Point out each malaria parasite and each leukocyte.
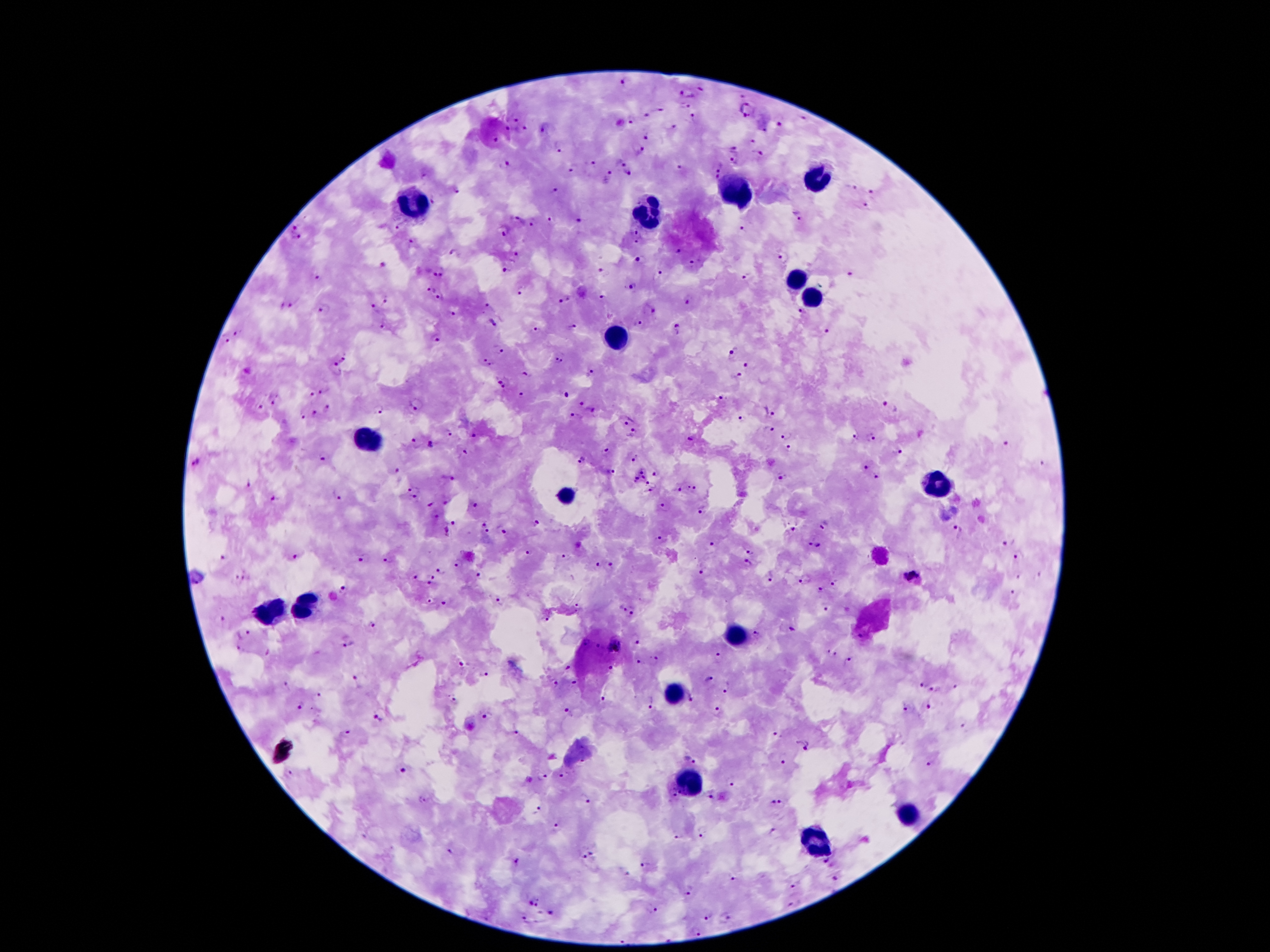
Approximate centers as [x, y] in pixels.
Malaria parasites: [627, 80], [702, 89], [688, 92], [739, 96], [685, 107], [748, 110], [664, 111], [647, 118], [805, 118], [515, 119], [632, 120], [694, 120], [781, 125], [672, 127], [506, 128], [544, 128], [522, 129], [647, 136], [496, 140], [751, 142], [558, 147], [734, 149], [640, 151], [758, 153], [621, 161], [734, 161], [593, 163], [503, 164], [718, 164], [574, 166], [677, 169], [629, 174], [424, 176], [607, 177], [714, 179], [852, 188], [457, 190], [557, 191], [873, 192], [435, 200], [866, 206], [798, 215], [518, 218], [552, 220], [580, 220], [532, 222], [399, 227], [504, 230], [742, 231], [297, 233], [639, 236], [411, 243], [676, 252], [455, 253], [516, 253], [783, 257], [640, 261], [383, 266], [695, 266], [506, 270], [603, 270], [439, 271], [662, 274], [849, 275], [750, 276], [321, 278], [634, 285], [431, 288], [520, 289], [441, 297], [602, 299], [688, 299], [386, 300], [564, 300], [295, 303], [488, 304], [280, 306], [374, 307], [326, 308], [651, 310], [803, 312], [454, 313], [493, 322], [385, 324], [639, 325], [570, 326], [677, 330], [535, 331], [239, 332], [824, 333], [226, 339], [437, 339], [499, 350], [732, 350], [343, 359], [560, 359], [748, 360], [489, 361], [335, 369], [592, 372], [525, 375], [736, 376], [503, 383], [326, 389], [524, 394], [311, 396], [564, 396], [723, 398], [276, 401], [419, 402], [582, 405], [260, 407], [329, 407], [890, 408], [592, 409], [377, 410], [772, 410], [316, 416], [576, 417], [301, 418], [626, 419], [744, 419], [769, 428], [450, 434], [633, 434], [785, 435], [474, 436], [854, 437], [692, 438], [870, 438], [418, 443], [432, 444], [1007, 444], [790, 450], [608, 452], [899, 452], [465, 453], [636, 456], [326, 457], [582, 461], [195, 462], [1041, 465], [866, 468], [643, 469], [398, 471], [611, 472], [657, 473], [782, 475], [877, 477], [448, 478], [643, 478], [636, 479], [652, 484], [695, 487], [680, 488], [415, 490], [337, 493], [649, 493], [273, 500], [448, 501], [431, 503], [477, 503], [664, 506], [702, 510], [481, 523], [534, 524], [824, 525], [450, 529], [792, 529], [505, 530], [958, 530], [490, 531], [661, 537], [1003, 544], [713, 545], [813, 545], [750, 551], [530, 552], [1019, 556], [566, 557], [295, 558], [362, 558], [222, 559], [390, 559], [458, 563], [598, 563], [748, 563], [612, 565], [440, 570], [702, 571], [910, 575], [481, 576], [772, 576], [416, 577], [432, 577], [1018, 577], [1040, 577], [240, 578], [805, 579], [836, 582], [431, 584], [345, 588], [822, 589], [1012, 593], [499, 599], [429, 602], [445, 604], [578, 606], [825, 608], [622, 609], [633, 611], [548, 616], [221, 618], [373, 622], [791, 628], [243, 632], [756, 633], [860, 635], [635, 638], [348, 642], [585, 642], [614, 645], [596, 647], [240, 649], [833, 653], [718, 658], [638, 661], [654, 661], [847, 661], [462, 664], [610, 668], [567, 669], [486, 675], [709, 680], [574, 682], [356, 683], [920, 683], [556, 685], [288, 686], [956, 686], [728, 687], [936, 688], [320, 695], [604, 695], [452, 699], [693, 699], [652, 700], [299, 705], [929, 707], [568, 709], [718, 709], [909, 710], [486, 716], [379, 717], [347, 732], [514, 734], [777, 734], [802, 745], [690, 760], [582, 762], [784, 762], [929, 765], [403, 770], [291, 774], [564, 775], [541, 777], [731, 786], [672, 793], [709, 796], [585, 798], [422, 799], [773, 801], [782, 804], [539, 808], [559, 827], [702, 835], [676, 838], [587, 856], [515, 859], [827, 860], [646, 864], [624, 872], [733, 878], [835, 878], [791, 885], [689, 892], [795, 902], [534, 903], [654, 909], [551, 915], [708, 916], [725, 918], [525, 920], [697, 932].
Leukocytes: [815, 177], [734, 193], [409, 205], [647, 213], [795, 280], [811, 293], [615, 339], [372, 443], [938, 484], [566, 495], [302, 604], [275, 609], [736, 632], [674, 691], [692, 784], [910, 814], [815, 843].

patient malaria status = positive for Plasmodium falciparum
capture = smartphone camera through the microscope eyepiece
field of view = single
image size = 1270×952 pixels
stain = Giemsa
magnification = 100x
preparation = thick peripheral-blood smear